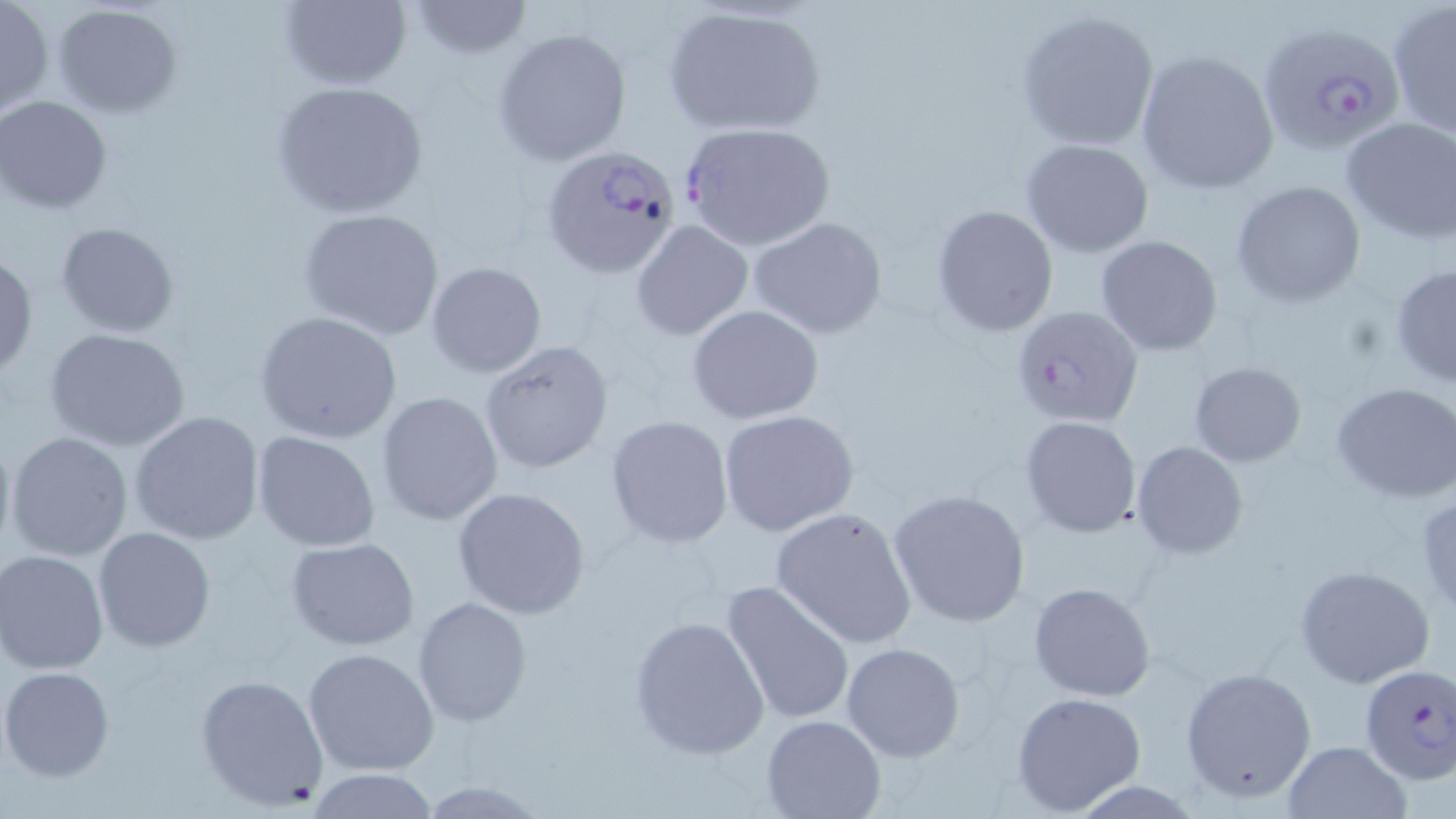
slide-level diagnosis = Plasmodium falciparum
field of view = single
modality = optical microscopy
magnification = 1000x
Plasmodium falciparum-infected red blood cell locations = approximate bounding boxes as (x1,y1)-(x2,y2) corner pairs in pixels: (1256,21)-(1406,158), (678,121)-(837,253), (542,144)-(684,280), (1010,305)-(1144,429), (1358,664)-(1456,784)
preparation = thin blood smear
uninfected red blood cell locations = approximate bounding boxes as (x1,y1)-(x2,y2) corner pairs in pixels: (0,0)-(51,115), (277,0)-(413,90), (406,1)-(533,58), (51,3)-(184,116), (661,4)-(827,136), (1387,4)-(1456,137), (1015,8)-(1161,150), (493,27)-(631,165), (1134,51)-(1280,194), (271,80)-(431,221), (0,96)-(112,213), (1340,118)-(1456,244), (1021,138)-(1154,257), (1231,180)-(1366,306), (932,204)-(1059,336), (297,207)-(446,339), (749,216)-(889,339), (630,219)-(754,341), (55,221)-(180,336), (1095,234)-(1224,356), (0,251)-(38,378), (425,261)-(547,378), (1389,264)-(1456,388), (687,304)-(823,423), (255,311)-(403,443), (44,326)-(191,452), (479,340)-(613,475), (1189,361)-(1307,466), (1331,382)-(1456,502), (376,390)-(504,526), (718,409)-(859,535), (130,410)-(266,545), (605,416)-(733,547), (1019,416)-(1143,537), (0,421)-(16,567), (5,430)-(133,563), (252,431)-(381,551), (1132,441)-(1248,558), (452,486)-(592,619), (888,488)-(1031,627), (1416,491)-(1456,616), (770,506)-(918,648), (94,527)-(217,652), (286,538)-(421,651), (0,549)-(109,674), (1294,564)-(1436,688), (722,580)-(856,726), (1028,582)-(1157,702), (412,595)-(532,727), (629,614)-(770,760), (841,642)-(965,763), (303,647)-(440,776), (1,666)-(115,781), (1179,666)-(1318,804), (194,673)-(329,810), (1011,692)-(1147,815), (762,713)-(886,819), (1281,740)-(1412,819), (302,770)-(441,819), (418,779)-(547,817), (1069,780)-(1204,817)
image size = 1456×819 pixels
stain = May-Grünwald-Giemsa